Comment on the morphology of the erythrocytes.
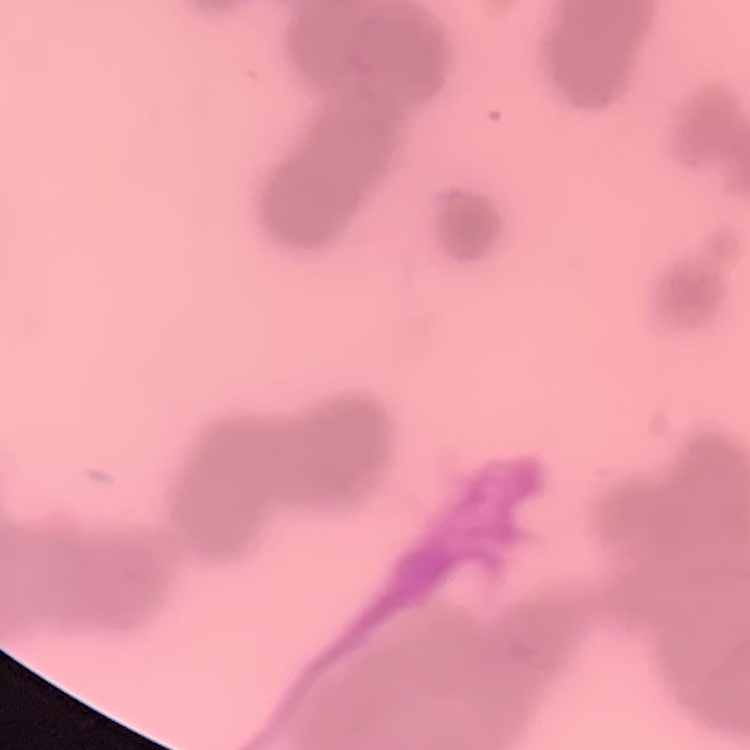
Rouleaux formation.

Summary:
  - Image type: square crop of a larger photomicrograph
  - Preparation: thin peripheral smear
  - Stain: Field's or Giemsa